Name the blood parasite species.
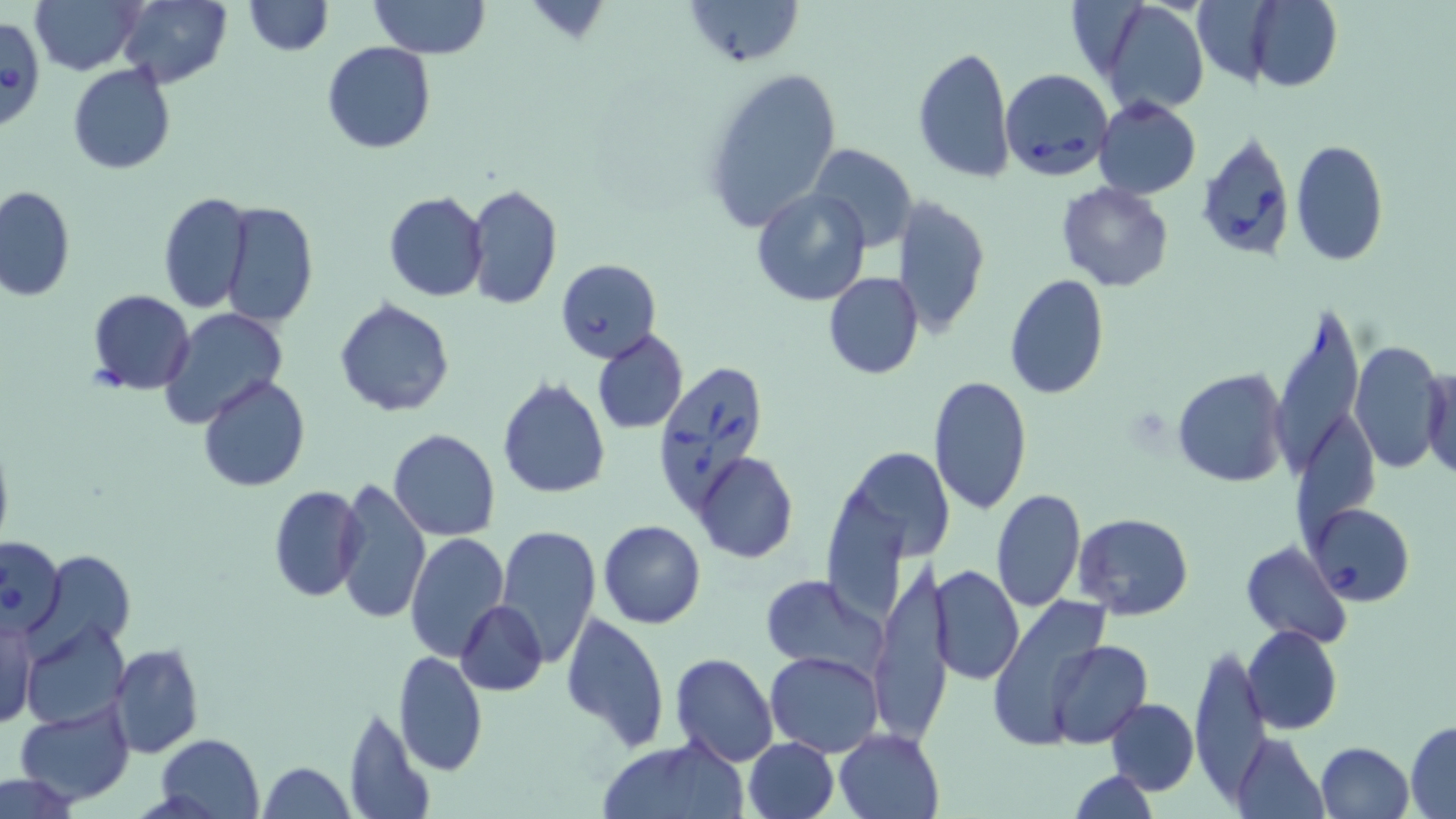

Babesia divergens.

Approximate bounding boxes as [x1, y1, x2, y2] in pixels. Babesia divergens-infected red blood cell locations: [1, 15, 47, 133], [1001, 69, 1113, 183], [1195, 129, 1299, 261], [652, 356, 771, 511], [1309, 503, 1415, 606], [1, 536, 66, 636]. Uninfected red blood cell locations: [29, 0, 145, 74], [117, 0, 231, 88], [243, 0, 332, 56], [370, 0, 490, 59], [681, 0, 802, 68], [1188, 0, 1278, 88], [1249, 0, 1342, 91], [1096, 2, 1209, 117], [321, 42, 437, 154], [912, 44, 1015, 183], [67, 64, 176, 175], [701, 64, 844, 235], [1094, 96, 1202, 198], [1290, 139, 1388, 265], [809, 143, 917, 251], [1055, 181, 1175, 293], [465, 183, 562, 311], [1, 185, 75, 303], [752, 186, 871, 307], [384, 191, 489, 301], [158, 192, 254, 313], [892, 197, 991, 339], [220, 200, 318, 327], [556, 258, 661, 363], [824, 272, 924, 379], [1002, 274, 1109, 399], [87, 290, 195, 395], [334, 298, 455, 418], [1272, 303, 1364, 482], [162, 309, 286, 423], [592, 329, 689, 434], [1348, 339, 1445, 477], [1421, 365, 1455, 482], [1173, 369, 1289, 487], [928, 374, 1033, 517], [199, 375, 309, 492], [497, 376, 610, 499], [1295, 415, 1376, 548], [389, 429, 500, 541], [842, 447, 949, 561], [694, 452, 798, 562], [334, 478, 430, 625], [267, 486, 365, 602], [991, 489, 1086, 612], [1074, 513, 1194, 622], [599, 520, 706, 628], [496, 525, 601, 667], [405, 531, 510, 661], [1240, 540, 1352, 647], [36, 548, 135, 654], [932, 563, 1023, 685], [870, 565, 951, 743], [759, 575, 886, 679], [987, 598, 1116, 750], [455, 600, 547, 696], [558, 611, 671, 753], [0, 616, 39, 732], [22, 620, 129, 730], [1243, 624, 1343, 735], [1046, 640, 1150, 747], [109, 643, 203, 758], [1189, 645, 1272, 800], [393, 651, 489, 777], [766, 651, 883, 757], [669, 652, 777, 766], [1106, 697, 1198, 794], [13, 700, 136, 806], [341, 705, 434, 819], [1406, 721, 1456, 816], [835, 728, 944, 818], [1232, 732, 1328, 819], [154, 734, 266, 819], [742, 737, 839, 819], [594, 740, 747, 819], [1316, 740, 1415, 819], [257, 761, 353, 819], [1070, 770, 1159, 818], [0, 774, 83, 817]. May-Grünwald-Giemsa-stained preparation. Thin blood film. One field of a larger specimen. 1000x magnification. Optical microscopy. Image is 1456×819 pixels.